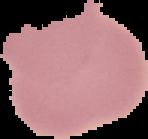

preparation = thin blood film
result = no Plasmodium parasites detected
image type = segmented cell region with the area outside set to black
image size = 148×139 pixels